Identify the blood parasite species.
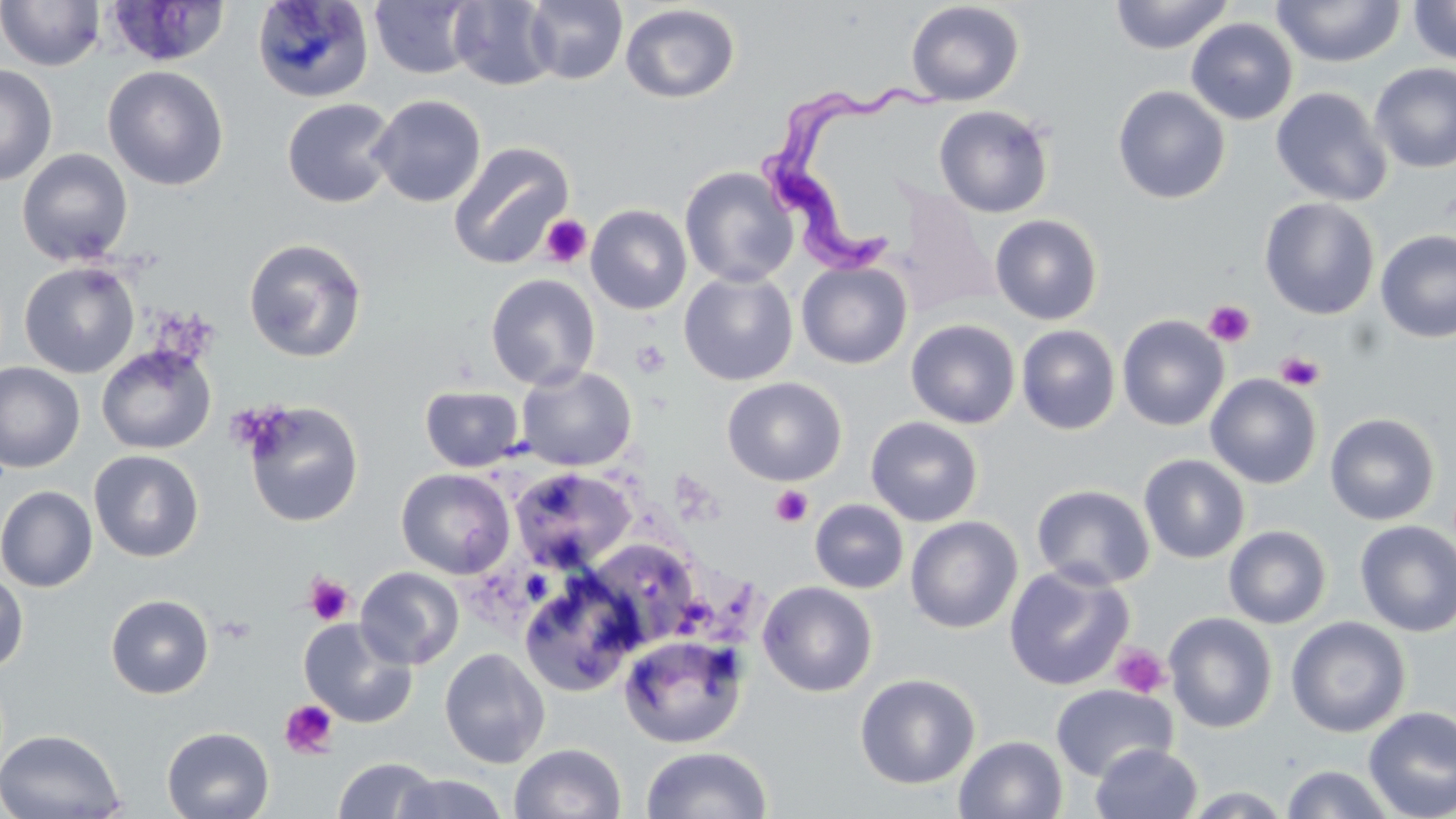

Trypanosoma brucei.

Summary:
  - Coordinate format: approximate bounding boxes as (x1, y1, x2, y2) in pixels
  - Trypanosoma brucei locations: (749, 81, 967, 282)
  - Platelet locations: (540, 215, 592, 267), (1204, 300, 1255, 348), (631, 339, 670, 377), (1276, 350, 1324, 391), (771, 485, 813, 527), (305, 574, 354, 626), (1110, 643, 1171, 699), (280, 699, 339, 759)
  - Uninfected red blood cell locations: (0, 0, 106, 71), (252, 0, 374, 104), (524, 0, 628, 85), (1109, 0, 1235, 54), (1407, 0, 1456, 66), (369, 1, 478, 79), (448, 1, 558, 90), (905, 1, 1025, 106), (1272, 1, 1405, 67), (106, 2, 231, 67), (619, 3, 741, 104), (1185, 18, 1298, 125), (1369, 62, 1456, 174), (0, 63, 58, 186), (102, 65, 229, 191), (1112, 85, 1231, 204), (1270, 87, 1393, 207), (370, 94, 486, 208), (281, 98, 398, 208), (933, 104, 1055, 218), (448, 142, 575, 269), (17, 148, 133, 266), (680, 166, 798, 287), (891, 186, 1000, 316), (1259, 197, 1380, 319), (586, 204, 692, 315), (990, 214, 1103, 325), (1375, 230, 1456, 343), (243, 238, 367, 363), (796, 260, 913, 369), (19, 261, 139, 378), (679, 271, 798, 385), (485, 273, 600, 390), (1117, 314, 1229, 431), (905, 318, 1020, 429), (1016, 324, 1121, 435), (96, 344, 216, 455), (0, 362, 85, 473), (516, 365, 636, 471), (1204, 373, 1322, 489), (722, 377, 846, 486), (420, 384, 524, 472), (242, 400, 364, 527), (1324, 413, 1440, 526), (865, 416, 983, 526), (89, 449, 204, 562), (1138, 454, 1250, 563), (510, 467, 637, 573), (396, 468, 515, 578), (1031, 484, 1155, 591), (0, 486, 98, 592), (810, 499, 909, 593), (905, 516, 1023, 633), (1354, 520, 1456, 637), (1223, 524, 1332, 629), (583, 537, 706, 648), (1004, 564, 1134, 691), (355, 566, 465, 669), (0, 571, 29, 673), (518, 572, 643, 696), (757, 580, 878, 697), (105, 594, 214, 699), (1164, 612, 1277, 734), (1286, 616, 1411, 737), (299, 617, 418, 728), (618, 634, 747, 750), (439, 647, 551, 768), (854, 673, 980, 789), (1050, 684, 1179, 781), (1363, 706, 1456, 819), (161, 726, 275, 819), (0, 728, 126, 818), (954, 735, 1068, 819), (509, 743, 627, 819), (1090, 743, 1203, 819), (640, 745, 774, 819), (332, 756, 439, 818), (1280, 764, 1397, 819), (391, 772, 509, 819), (1178, 786, 1297, 818)
  - Modality: optical microscopy
  - Stain: May-Grünwald-Giemsa
  - Field of view: single
  - Magnification: 1000x
  - Preparation: thin blood smear
  - Image size: 1456×819 pixels